State the preparation type.
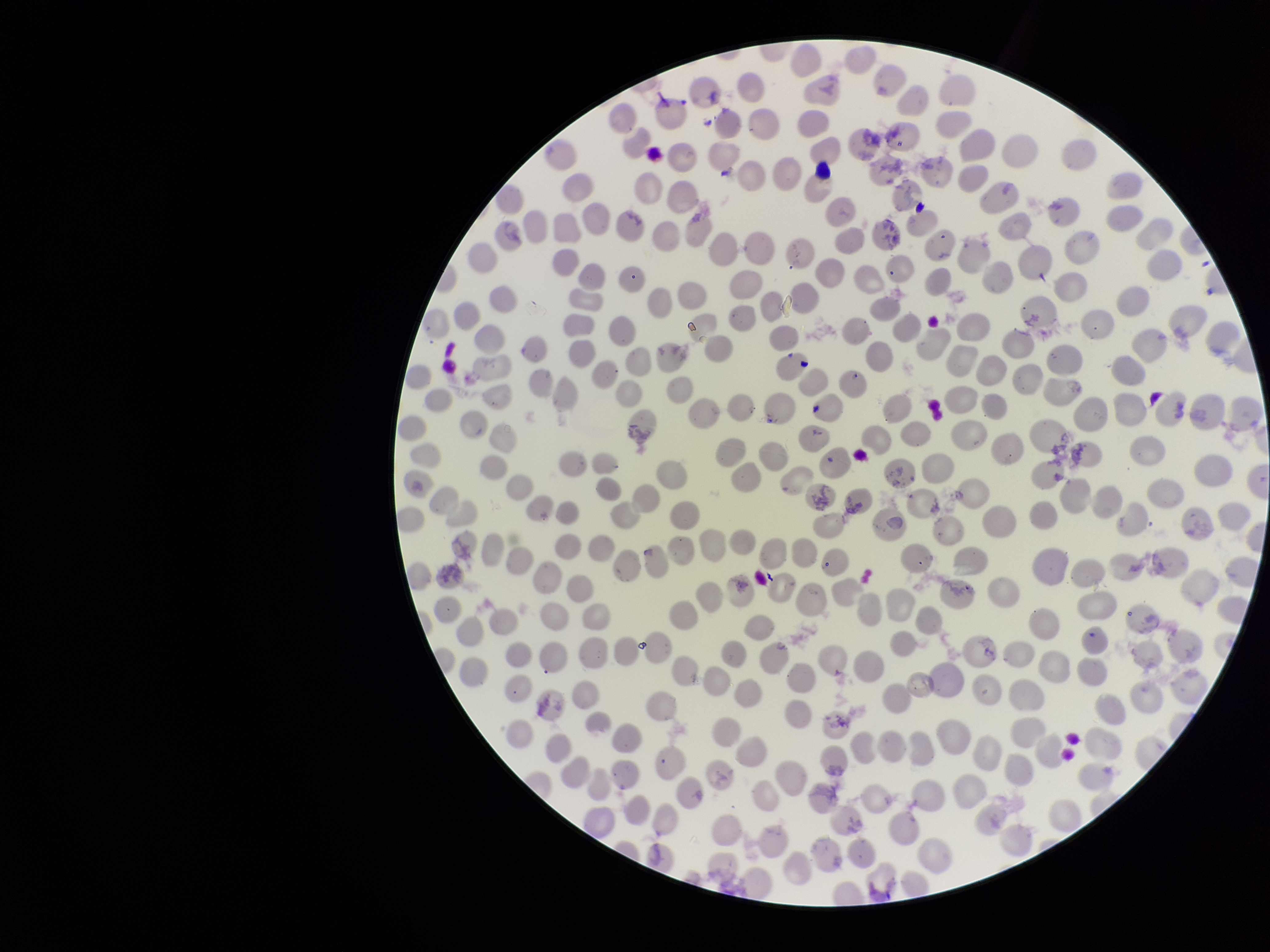
A thin smear.

patient malaria status = positive
red blood cell count = 271
capture = smartphone photograph through the microscope eyepiece
parasitized red blood cells = none identified
parasitized red blood cell count = 0
image size = 1270×952 pixels
stain = Giemsa
field of view = single
species reported for this patient = Plasmodium vivax